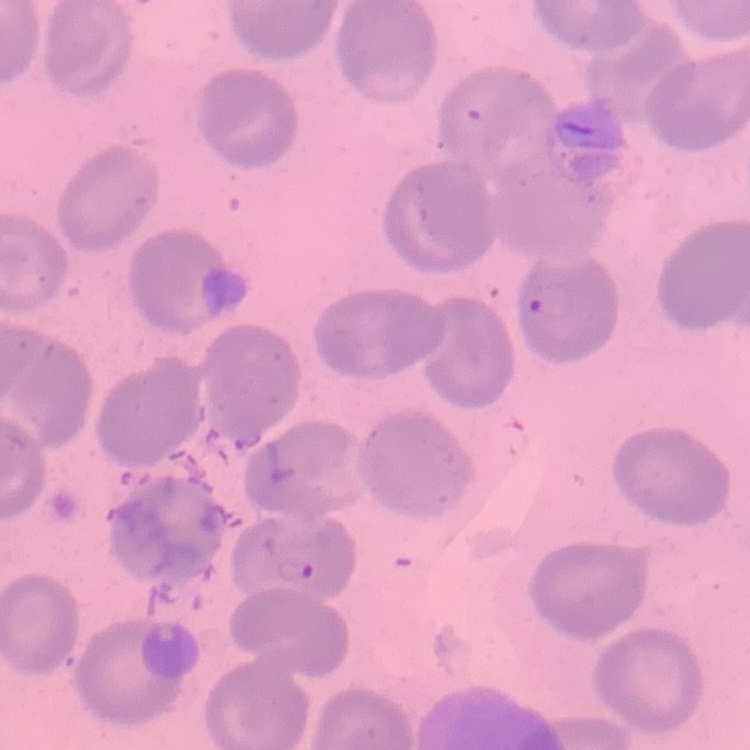
Summary:
  - Red blood cell morphology: no rouleaux formation
  - Preparation: thin blood film
  - Stain: Field's or Giemsa
  - Image type: square crop of a larger photomicrograph